Evaluate for malaria.
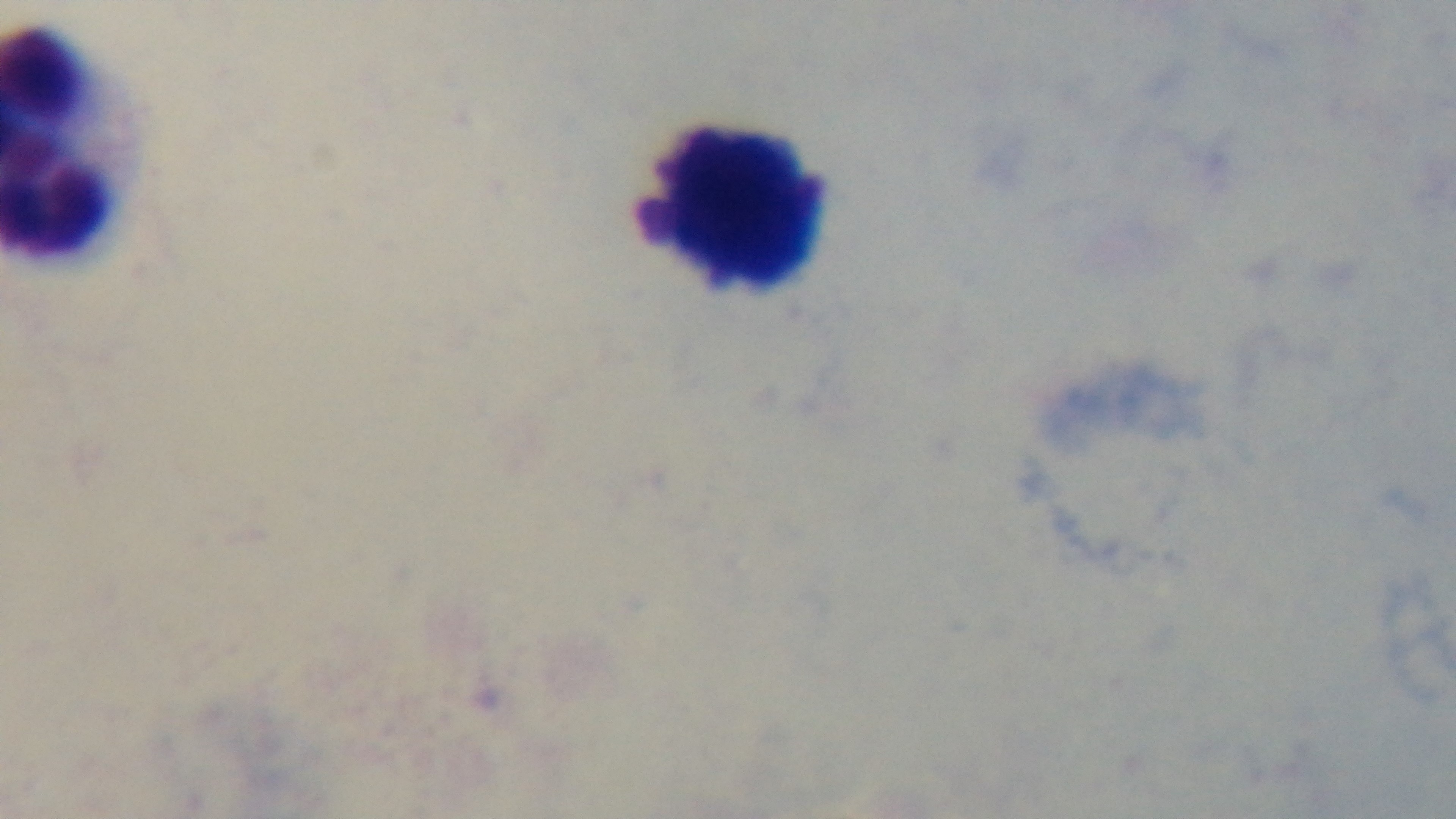
It is uninfected.

Summary:
  - Field of view: single
  - Objective: 100x oil immersion
  - Preparation: thick
  - Stain: Giemsa
  - Capture: mounted 4K digital camera
  - Modality: light microscopy